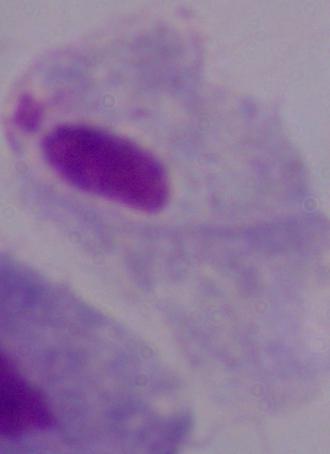
A trichomonad is seen. Captured at 1000x magnification. Micrograph.